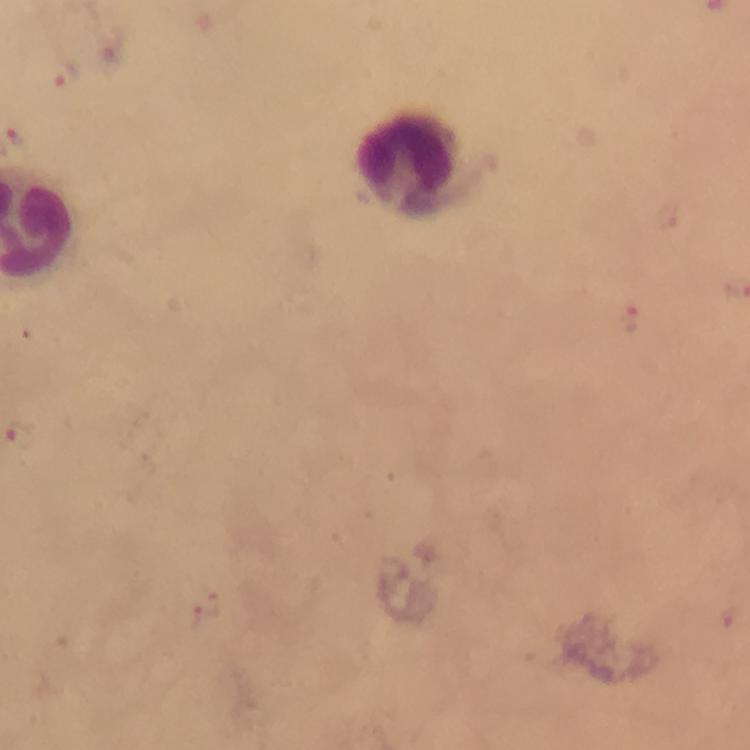

Approximate centers as (x, y) in pixels. Malaria parasite locations: (61, 77), (630, 314), (209, 612). Leukocyte locations: (417, 160). Image is 750×750 pixels. Photographed through the microscope with a smartphone camera. Immersion oil was used. Giemsa-stained preparation. Thick blood film. Cropped region of a single field of view. From a malaria diagnostic workup. 100x magnification.